Describe the morphology of the red blood cells.
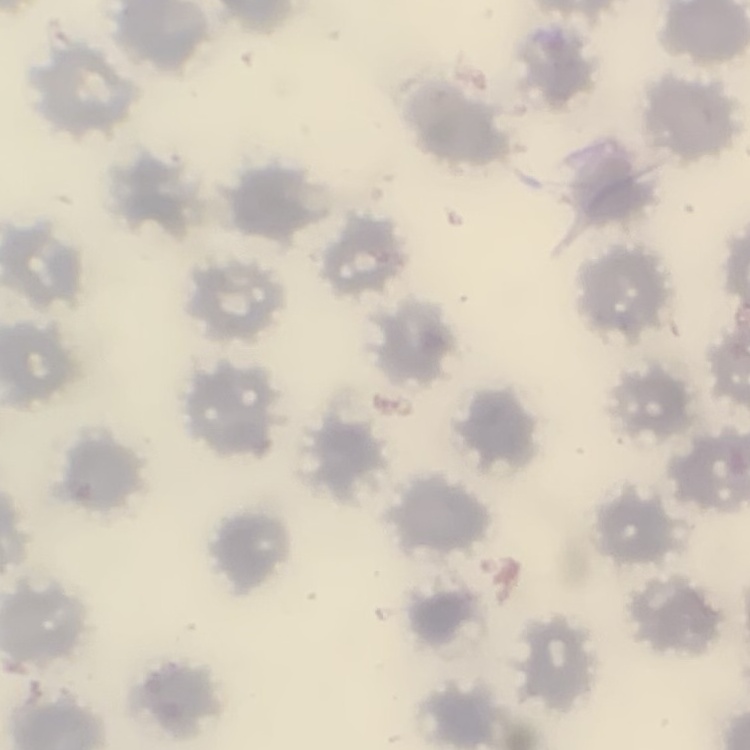
No rouleaux formation.

Summary:
  - Preparation: thin peripheral smear
  - Image type: square crop of a larger photomicrograph
  - Stain: Field's or Giemsa